Identify the parasite.
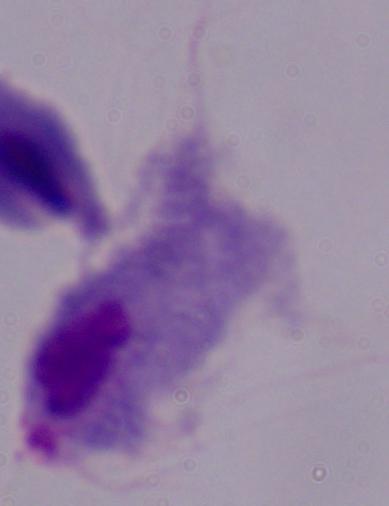
A trichomonad.

Summary:
  - Magnification: 1000x
  - Modality: micrograph